Report the malaria status of this cell.
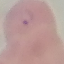
It is parasitized.

Automatically extracted cell patch, resized to 64 × 64 pixels. Photographed with a smartphone camera at the microscope eyepiece. Thin blood film. Giemsa-stained preparation.